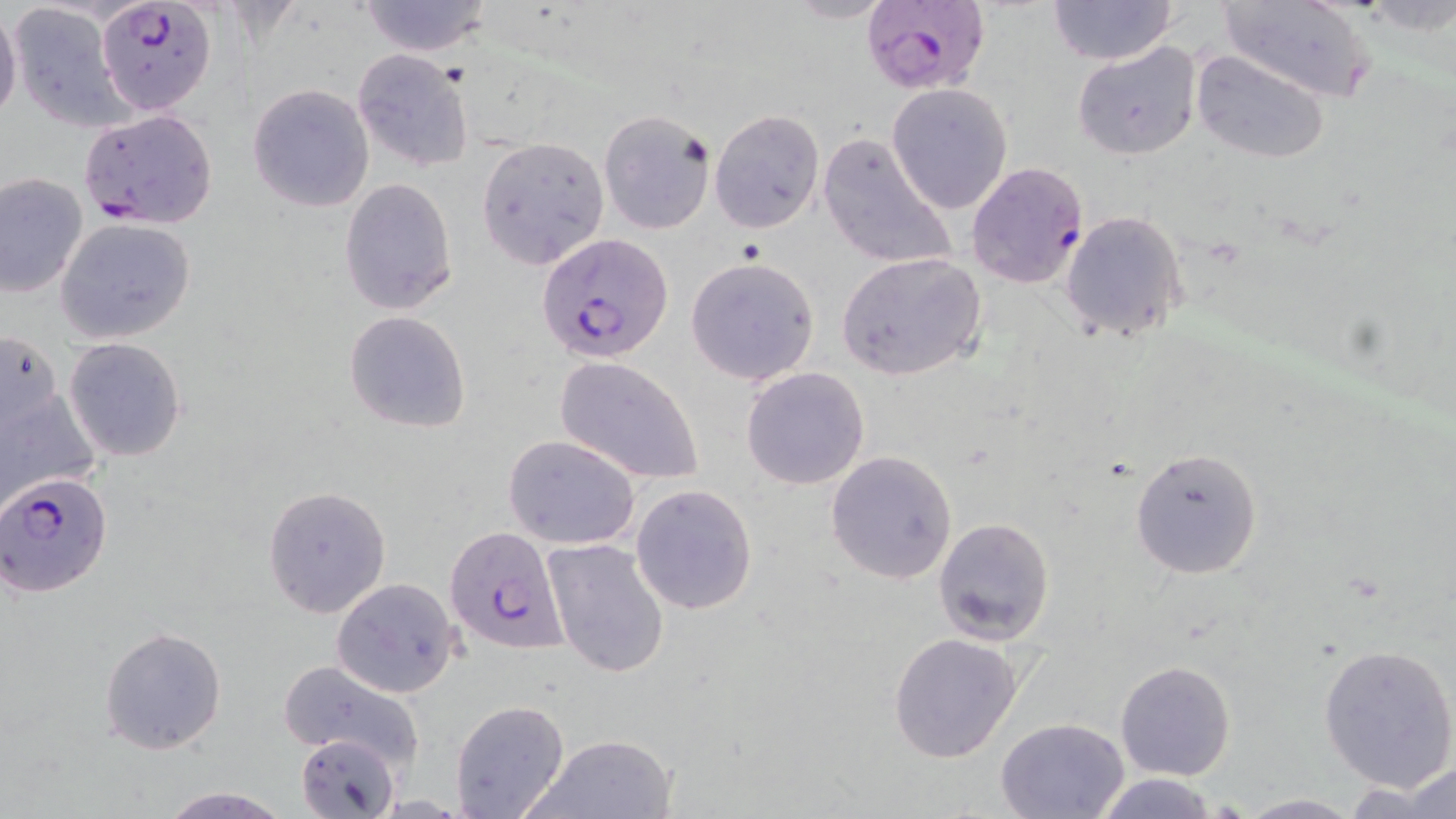 Approximate bounding boxes as (x1, y1, x2, y2) in pixels. Uninfected red blood cell locations: (355, 0, 495, 58), (1048, 0, 1178, 65), (1218, 0, 1376, 102), (781, 1, 898, 24), (4, 5, 129, 131), (0, 7, 22, 125), (1072, 41, 1202, 161), (1191, 49, 1332, 164), (352, 52, 473, 172), (885, 82, 1014, 215), (247, 83, 375, 212), (709, 109, 825, 233), (598, 110, 715, 235), (816, 130, 958, 274), (476, 136, 610, 270), (0, 173, 89, 298), (338, 177, 459, 316), (1060, 211, 1187, 341), (57, 217, 196, 342), (836, 252, 987, 381), (684, 256, 821, 386), (343, 310, 471, 432), (1, 325, 66, 454), (64, 337, 187, 462), (553, 356, 705, 485), (0, 365, 100, 516), (740, 367, 870, 489), (503, 435, 639, 550), (1130, 448, 1262, 577), (825, 451, 957, 584), (630, 483, 758, 616), (263, 486, 393, 619), (934, 518, 1056, 645), (542, 538, 670, 679), (330, 578, 462, 697), (99, 625, 227, 755), (887, 630, 1024, 762), (1317, 641, 1456, 792), (1115, 660, 1235, 781), (277, 662, 425, 772), (449, 700, 570, 819), (995, 717, 1133, 818), (297, 732, 402, 818), (526, 732, 677, 818), (1403, 761, 1456, 817), (1086, 773, 1225, 817), (1351, 777, 1449, 816), (155, 786, 295, 819), (1236, 793, 1363, 818). Plasmodium falciparum-infected red blood cell locations: (859, 0, 985, 93), (95, 2, 216, 115), (78, 108, 219, 229), (966, 162, 1090, 290), (526, 231, 660, 357), (2, 471, 112, 598), (445, 523, 568, 653). Slide-level diagnosis: Plasmodium falciparum. Optical microscopy. Thin blood smear. May-Grünwald-Giemsa-stained preparation. Captured at 1000x magnification. Single field of view. Image is 1456×819 pixels.